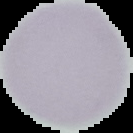 Cell region segmented out of the field of view; the surrounding area is masked to black. Image is 133×133 pixels. From a thin blood smear. Result: no malaria parasites seen.